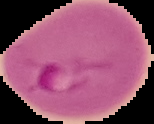
Summary:
  - Result: Plasmodium parasites detected
  - Preparation: thin blood film
  - Image size: 154×124 pixels
  - Image type: cell region segmented out of the field of view; surrounding area masked to black